Assess this cell for malaria.
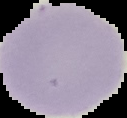

It is uninfected.

Summary:
  - Preparation: thin blood film
  - Image size: 127×118 pixels
  - Image type: segmented cell region on a black background